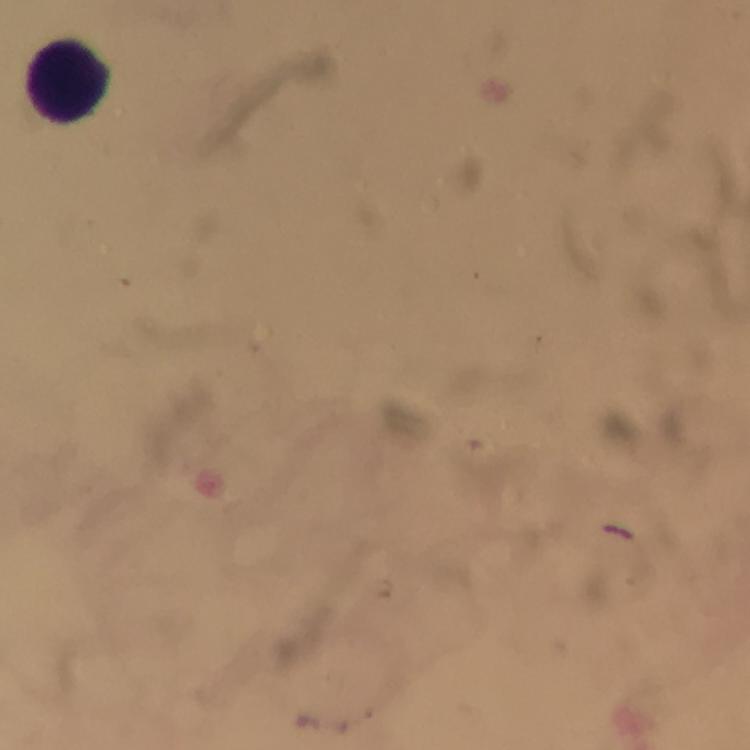

Approximate centers as (x, y) in pixels.
Summary:
  - Leukocyte locations: (69, 82)
  - Image size: 750×750 pixels
  - Stain: Giemsa
  - Magnification: 100x
  - Cropped from: a single field of view
  - Preparation: thick blood smear
  - Context: from a diagnostic examination for malaria
  - Immersion oil: used
  - Malaria parasites: none seen
  - Capture: smartphone camera through the microscope